State the preparation type.
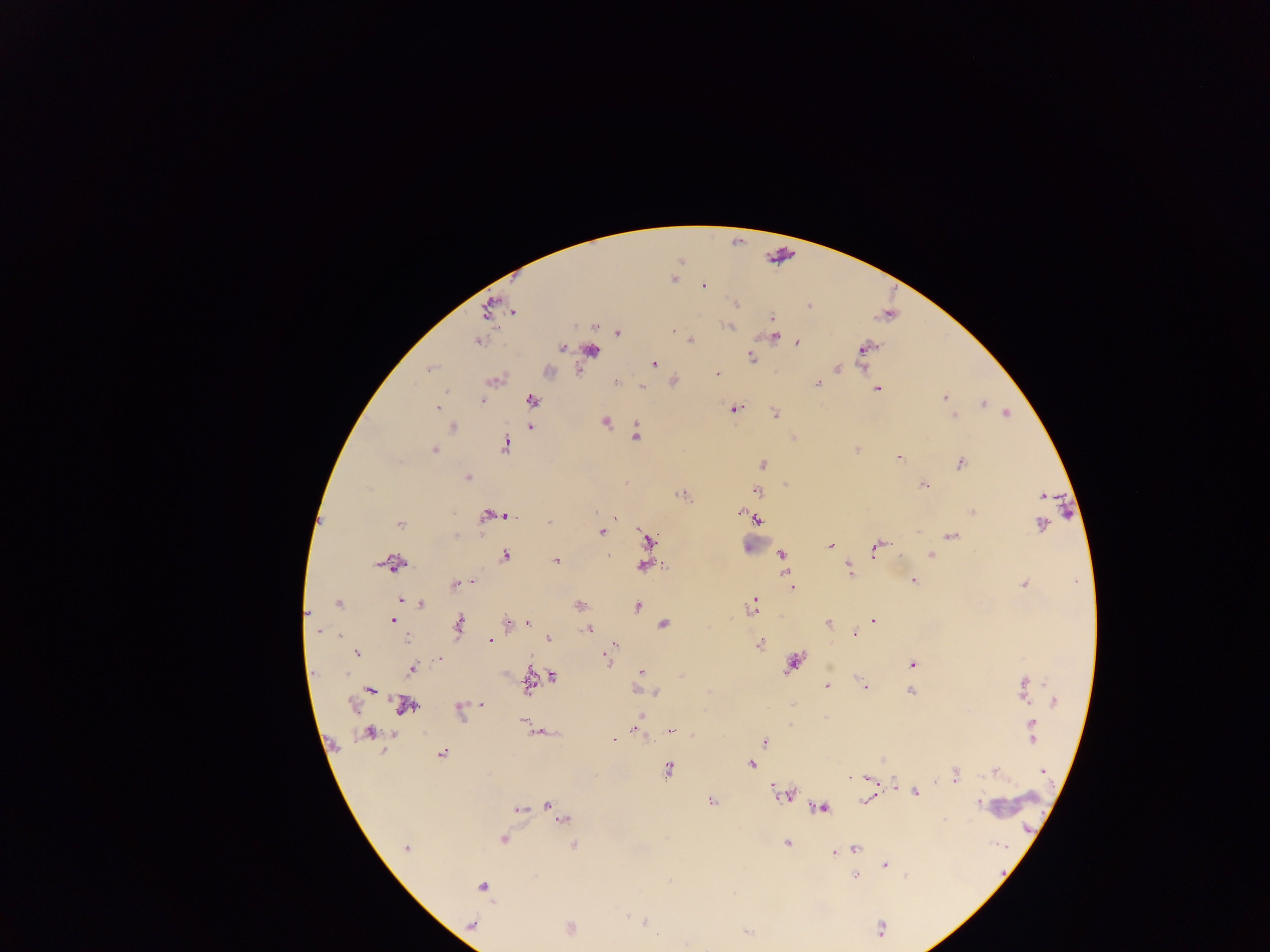

Thick blood film.

leukocyte locations = approximate centers as (x, y) in pixels: (781, 254), (592, 352), (755, 545), (1013, 806)
country = Ghana
malaria parasite locations = approximate centers as (x, y) in pixels: (672, 280), (703, 286), (735, 303), (809, 305), (488, 308), (512, 312), (772, 318), (595, 326), (729, 326), (672, 331), (618, 333), (775, 336), (690, 340), (477, 341), (797, 342), (562, 348), (865, 348), (751, 356), (654, 364), (430, 368), (837, 368), (717, 374), (673, 381), (615, 382), (819, 383), (641, 386), (877, 388), (446, 391), (944, 397), (481, 401), (532, 401), (983, 404), (438, 407), (735, 409), (1006, 413), (775, 414), (954, 416), (605, 421), (453, 427), (532, 427), (637, 435), (505, 445), (857, 449), (433, 451), (899, 458), (762, 464), (961, 464), (467, 478), (923, 485), (757, 491), (682, 495), (1042, 495), (973, 511), (596, 512), (742, 512), (505, 514), (491, 515), (614, 518), (756, 519), (549, 522), (400, 524), (1041, 524), (602, 532), (952, 535), (647, 539), (830, 545), (875, 548), (781, 555), (931, 555), (505, 556), (608, 556), (556, 561), (395, 563), (643, 566), (849, 569), (913, 580), (472, 582), (1024, 584), (455, 585), (792, 588), (401, 600), (338, 603), (421, 605), (580, 605), (753, 605), (637, 606), (393, 621), (873, 621), (508, 622), (829, 623), (528, 624), (664, 624), (459, 625), (589, 629), (318, 632), (855, 633), (339, 636), (407, 638), (548, 638), (489, 640), (615, 644), (760, 644), (611, 650), (357, 653), (440, 659), (606, 659), (793, 663), (912, 664), (410, 669), (641, 672), (552, 676), (827, 686), (864, 687), (1025, 687), (370, 690), (638, 690), (910, 691), (654, 692), (1054, 702), (482, 704), (353, 706), (405, 706), (459, 710), (640, 716), (523, 720), (1032, 726), (637, 731), (671, 731), (368, 734), (613, 739), (765, 742), (441, 753), (751, 764), (669, 769), (995, 771), (1043, 771), (956, 775), (867, 778), (915, 793), (783, 794), (866, 800), (712, 802), (978, 803), (549, 806), (822, 808), (518, 810), (555, 811), (561, 817), (503, 839), (787, 843), (574, 844), (407, 847), (855, 849), (835, 853), (885, 864), (855, 877), (906, 877), (669, 880), (481, 886), (646, 921), (472, 925), (880, 929), (747, 933), (657, 936)
image size = 1270×952 pixels
capture = mobile-phone photograph through a microscope
field of view = single